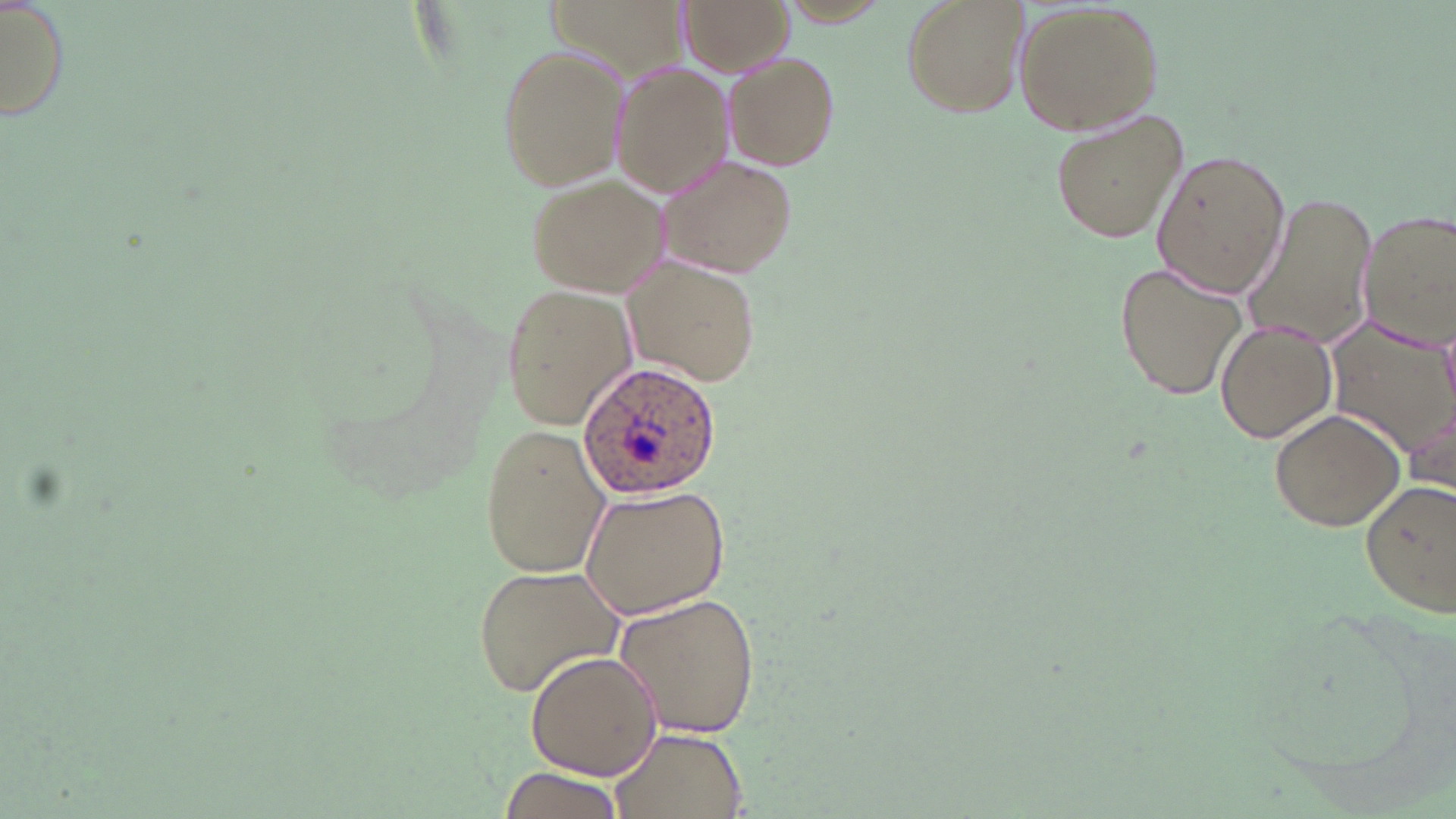
Approximate bounding boxes as (x1,y1)-(x2,y2) corner pairs in pixels. Uninfected red blood cell locations: (679,0)-(796,76), (899,0)-(1031,118), (1015,1)-(1166,137), (1,3)-(72,126), (493,44)-(628,189), (724,53)-(840,170), (610,64)-(736,198), (1047,107)-(1191,246), (1152,150)-(1290,299), (654,154)-(800,278), (525,172)-(667,297), (1240,191)-(1380,350), (1358,209)-(1456,349), (622,257)-(765,389), (1114,260)-(1249,400), (500,284)-(638,428), (1215,320)-(1337,443), (1327,325)-(1456,462), (1404,403)-(1456,503), (1270,406)-(1407,533), (479,424)-(611,579), (1358,477)-(1456,619), (576,484)-(731,620), (474,564)-(627,697), (610,592)-(762,737), (524,647)-(662,779), (608,726)-(751,818), (499,768)-(625,817). Plasmodium ovale-infected red blood cell locations: (576,358)-(723,503). Slide-level diagnosis: Plasmodium ovale. Image is 1456×819 pixels. May-Grünwald-Giemsa-stained preparation. Light microscopy. Single field of view. Thin blood smear. 1000x magnification.